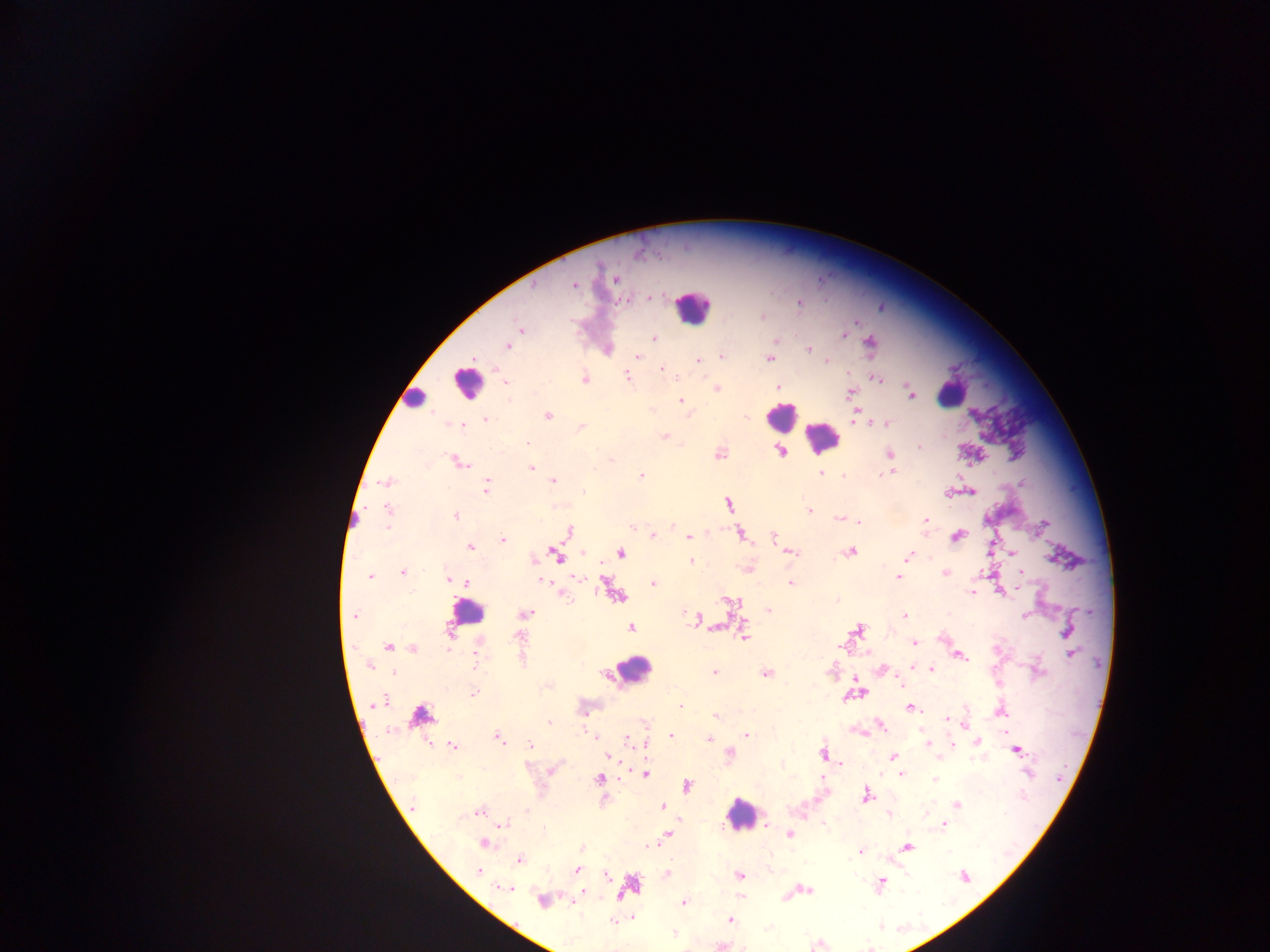

Approximate centers as [x, y] in pixels. Leukocyte locations: [690, 311], [465, 384], [956, 392], [420, 396], [779, 417], [820, 441], [466, 613], [635, 668], [741, 823]. Malaria parasite locations (subset; some below the resolvable size): [635, 255], [615, 281], [573, 285], [535, 287], [648, 297], [626, 301], [799, 303], [761, 315], [520, 328], [848, 333], [845, 337], [655, 338], [775, 340], [509, 347], [808, 347], [608, 348], [721, 354], [638, 356], [770, 359], [698, 360], [826, 360], [662, 369], [627, 375], [584, 378], [877, 378], [506, 381], [780, 386], [718, 388], [852, 392], [911, 396], [679, 400], [652, 409], [858, 409], [548, 417], [486, 418], [447, 423], [886, 423], [465, 424], [868, 424], [581, 426], [662, 435], [527, 442], [919, 446], [890, 454], [460, 462], [532, 469], [821, 472], [893, 472], [641, 474], [844, 474], [385, 482], [553, 482], [487, 487], [581, 489], [385, 506], [810, 511], [456, 515], [839, 519], [925, 519], [861, 521], [672, 526], [1042, 526], [386, 527], [630, 529], [654, 534], [688, 536], [502, 540], [470, 547], [1012, 553], [910, 556], [690, 561], [402, 573], [981, 573], [1020, 573], [946, 574], [369, 576], [897, 577], [448, 578], [456, 581], [541, 581], [465, 582], [654, 582], [789, 582], [1023, 588], [972, 592], [1001, 593], [561, 595], [837, 600], [526, 613], [1024, 614], [351, 615], [905, 615], [630, 627], [743, 638], [914, 642], [387, 646], [841, 647], [413, 649], [960, 656], [368, 667], [881, 669], [931, 669], [715, 672], [765, 673], [392, 674], [900, 685], [474, 692], [380, 702], [678, 706], [909, 710], [1002, 713], [715, 716], [946, 719], [549, 722], [964, 725], [582, 727], [670, 735], [747, 735], [594, 736], [498, 738], [708, 739], [627, 740], [953, 740], [926, 742], [978, 742], [529, 744], [453, 746], [1018, 750], [646, 751], [729, 753], [892, 756], [607, 757], [840, 765], [1030, 771], [1024, 773], [900, 775], [599, 779], [934, 779], [957, 803], [660, 805], [479, 812], [889, 816], [943, 823], [502, 825], [766, 825], [790, 836], [484, 843], [649, 845], [860, 851], [519, 861], [577, 868], [667, 871], [738, 875], [883, 880], [511, 888], [810, 891], [583, 892], [621, 896], [686, 900], [540, 901], [632, 917], [730, 919], [673, 932]. Image is 1270×952 pixels. Thick blood smear. One field of view. Sample from Ghana. Photographed through a microscope with a mobile-phone camera.